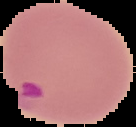 Image is 136×127 pixels. Malaria status: parasitized. Segmented cell region on a black background. From a thin blood film.